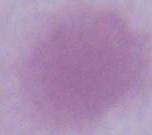

Summary:
  - Identification: red blood cell
  - Modality: photomicrograph
  - Magnification: 1000x